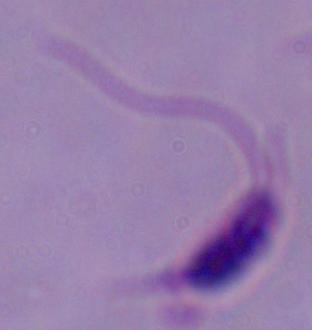
1000x magnification. Micrograph. A Leishmania parasite is seen.